Locate every leukocyte (white blood cell).
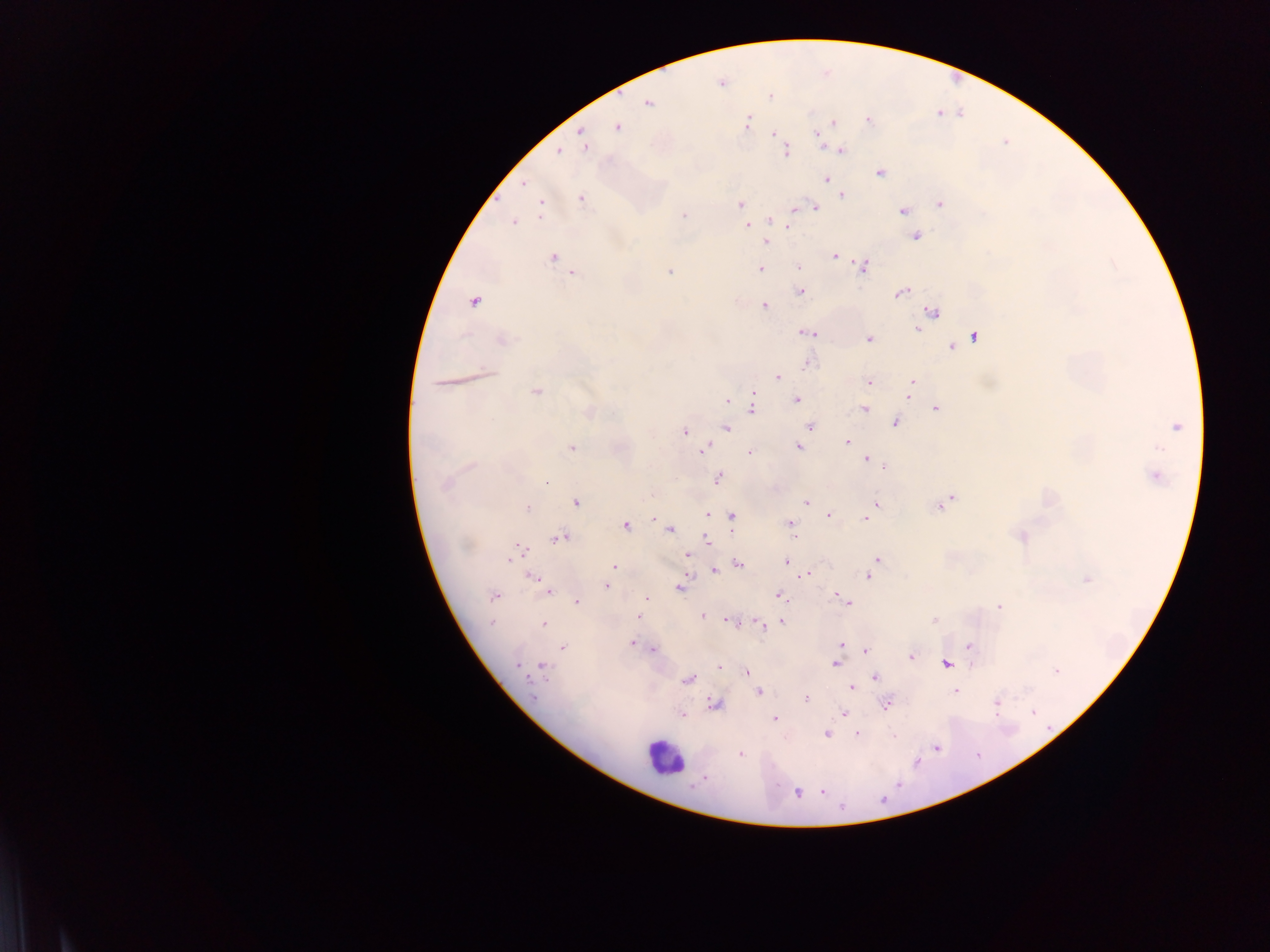

Approximate centers as x y in pixels.
Leukocytes: 664 757.

image size = 1270×952 pixels
preparation = thick blood smear
country = Ghana
capture = mobile-phone photograph through a microscope
field of view = single
Plasmodium parasite locations = approximate centers as x y in pixels: 721 83; 770 96; 649 103; 938 113; 868 120; 747 122; 833 122; 618 128; 773 134; 818 137; 583 142; 841 150; 557 151; 787 151; 880 173; 826 179; 524 183; 842 195; 581 198; 940 204; 739 205; 814 207; 541 208; 903 210; 684 215; 770 220; 513 222; 747 225; 788 226; 916 236; 766 242; 834 255; 553 257; 839 259; 864 266; 799 267; 760 270; 669 271; 572 273; 800 291; 901 293; 474 302; 765 306; 933 311; 919 329; 808 332; 974 337; 504 340; 869 340; 952 347; 807 364; 778 378; 441 382; 869 382; 913 382; 911 389; 537 391; 909 397; 797 399; 727 402; 752 404; 864 409; 936 409; 589 412; 895 423; 809 426; 1177 427; 726 429; 685 430; 847 442; 798 446; 572 448; 704 449; 749 453; 866 458; 469 467; 884 467; 1155 475; 719 478; 546 482; 446 484; 949 499; 576 502; 805 502; 876 504; 941 504; 527 507; 869 513; 707 514; 829 515; 731 517; 866 518; 790 524; 625 525; 669 529; 795 537; 1021 537; 560 538; 707 539; 465 546; 517 553; 687 555; 877 559; 787 562; 739 564; 614 567; 714 570; 807 573; 868 576; 534 578; 1087 579; 606 586; 680 587; 547 590; 779 595; 494 596; 646 598; 577 602; 844 602; 999 607; 637 616; 703 616; 935 620; 730 621; 781 622; 492 623; 543 624; 759 625; 632 643; 841 644; 969 645; 563 648; 653 650; 866 651; 911 656; 836 663; 947 663; 518 665; 543 666; 720 667; 747 671; 1056 671; 875 677; 688 680; 851 688; 955 691; 759 692; 806 698; 997 703; 715 705; 887 705; 1034 712; 844 713; 682 714; 775 720; 827 734; 857 735; 894 736; 936 749; 740 754; 822 791; 797 793